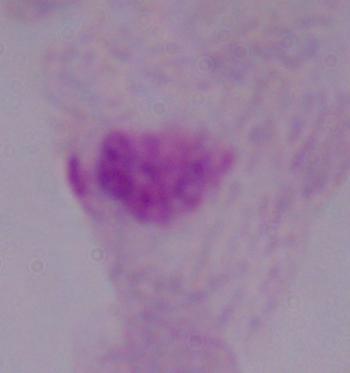

Captured at 1000x magnification. A trichomonad is shown. Micrograph.